Identify the parasite.
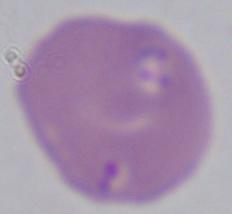

This is Babesia.

1000x magnification. Micrograph.